Outline each Plasmodium malariae-infected red blood cell.
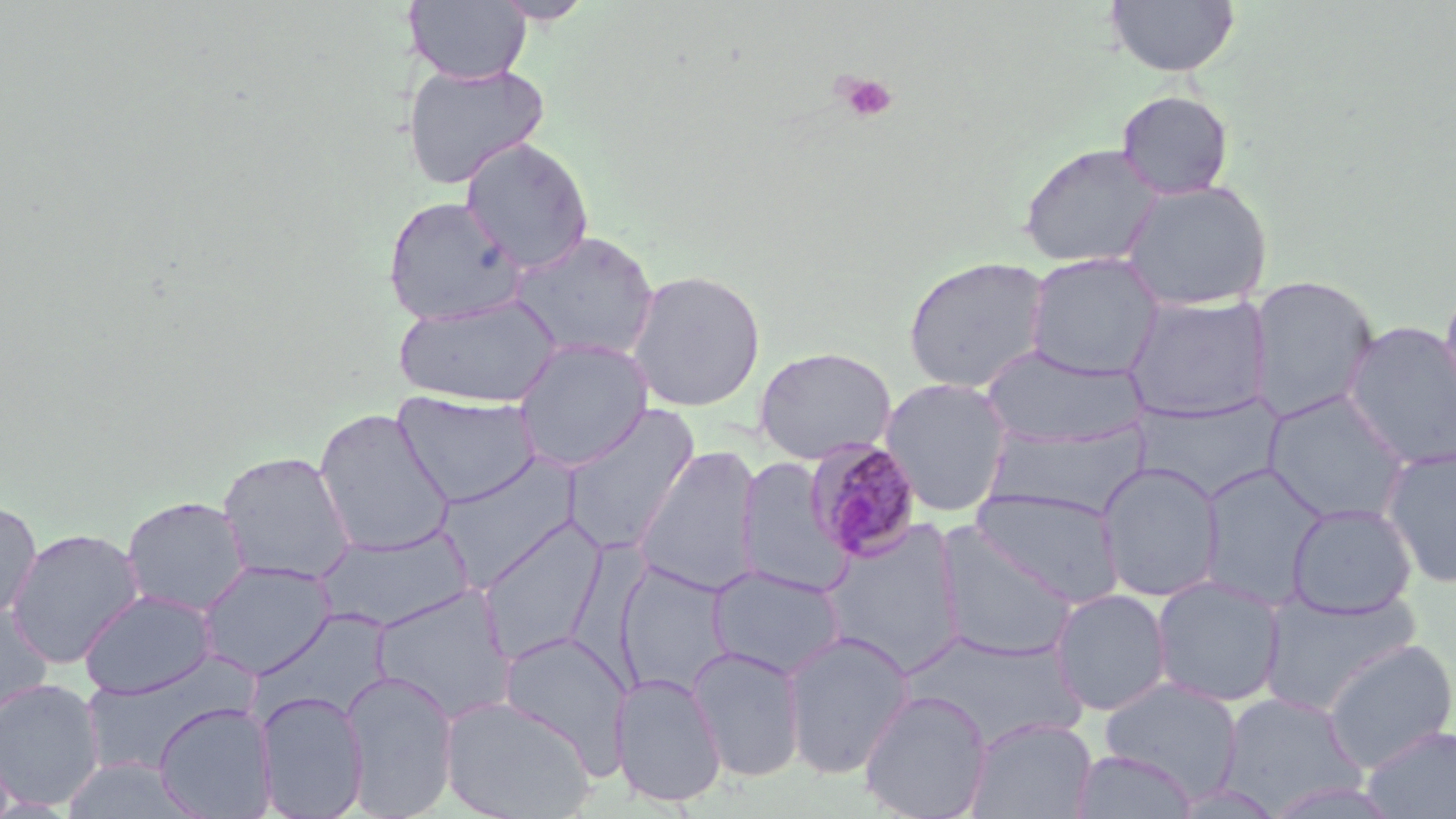

Approximate bounding boxes as [x1, y1, x2, y2] in pixels.
Plasmodium malariae-infected red blood cells: [803, 437, 924, 562].

Uninfected red blood cell locations: [404, 0, 531, 85], [491, 0, 596, 23], [1106, 0, 1240, 77], [401, 61, 549, 191], [1116, 90, 1235, 201], [460, 137, 594, 273], [1018, 141, 1164, 270], [1121, 180, 1274, 312], [382, 195, 526, 326], [509, 229, 659, 362], [1025, 253, 1166, 379], [902, 255, 1053, 393], [625, 268, 766, 412], [1247, 275, 1379, 422], [1439, 275, 1456, 418], [393, 293, 562, 409], [1122, 293, 1273, 423], [1341, 321, 1456, 470], [513, 338, 654, 472], [981, 343, 1147, 450], [754, 346, 896, 464], [879, 377, 1014, 517], [1262, 390, 1413, 524], [392, 391, 543, 508], [1134, 394, 1284, 502], [561, 403, 701, 555], [314, 408, 454, 557], [984, 420, 1149, 520], [634, 444, 762, 597], [1379, 446, 1456, 587], [217, 450, 357, 585], [437, 454, 581, 589], [737, 456, 849, 597], [1095, 462, 1224, 603], [1198, 463, 1327, 610], [969, 488, 1125, 607], [121, 495, 250, 616], [0, 499, 42, 622], [1287, 502, 1418, 618], [478, 516, 607, 665], [820, 520, 967, 675], [314, 524, 475, 633], [932, 524, 1077, 662], [6, 527, 145, 669], [197, 560, 336, 679], [615, 560, 735, 696], [707, 565, 847, 680], [1150, 576, 1285, 708], [370, 586, 516, 723], [1049, 588, 1173, 716], [79, 589, 217, 700], [1259, 592, 1420, 715], [0, 603, 53, 723], [781, 629, 915, 780], [898, 630, 1088, 753], [497, 631, 627, 772], [1320, 638, 1456, 773], [687, 645, 807, 783], [77, 661, 252, 776], [340, 669, 459, 818], [611, 672, 727, 808], [0, 678, 105, 810], [1099, 678, 1245, 800], [255, 689, 369, 818], [858, 689, 992, 819], [1219, 691, 1364, 812], [440, 695, 596, 819], [153, 702, 277, 819], [965, 716, 1097, 819], [1361, 724, 1456, 818], [1070, 749, 1198, 818], [58, 757, 203, 819], [1169, 780, 1289, 818]. Platelet locations: [835, 73, 898, 123]. Slide-level diagnosis: Plasmodium malariae. May-Grünwald-Giemsa stain. One field of a larger specimen. Light microscopy. 1000x magnification. Thin blood film. Image is 1456×819 pixels.